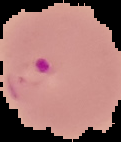

preparation = thin blood smear
malaria status = parasitized
image size = 121×142 pixels
image type = segmented cell region on a black background